Identify the parasite.
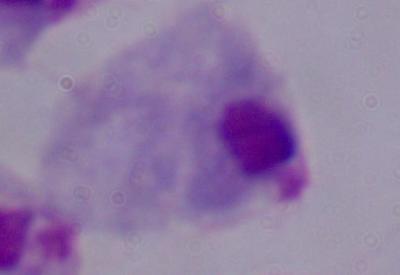
This is a trichomonad.

Summary:
  - Magnification: 1000x
  - Modality: photomicrograph